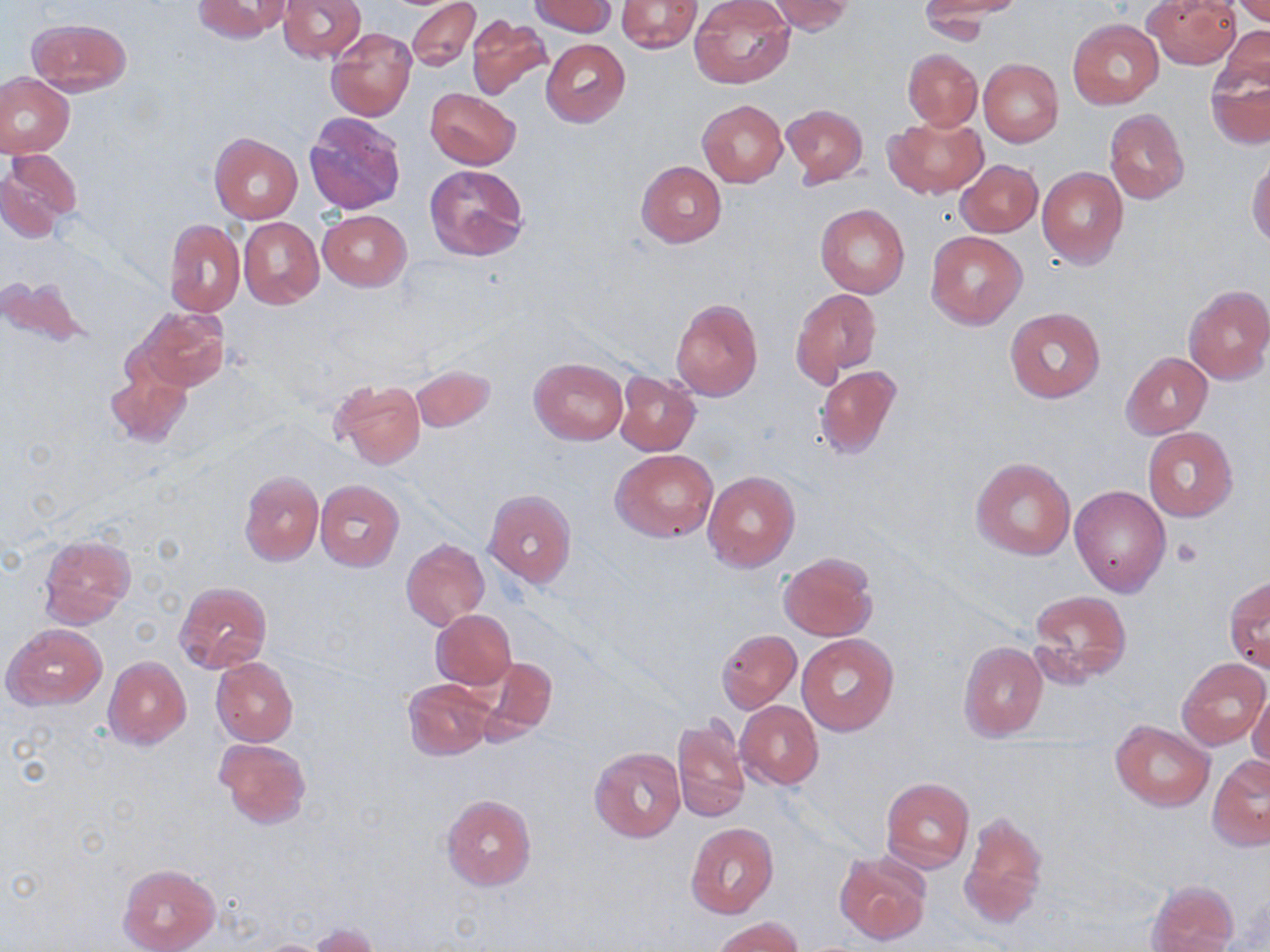

Summary:
  - Coordinate format: approximate bounding boxes as [x1, y1, x2, y2] in pixels
  - Uninfected red blood cell locations: [191, 0, 290, 43], [278, 0, 366, 63], [407, 0, 481, 72], [765, 0, 854, 35], [922, 0, 1026, 18], [1144, 0, 1241, 69], [1231, 0, 1270, 24], [529, 1, 615, 37], [616, 1, 702, 52], [689, 1, 794, 88], [917, 4, 1012, 41], [466, 14, 554, 102], [27, 17, 131, 96], [1068, 19, 1163, 109], [326, 27, 416, 121], [1214, 27, 1270, 96], [540, 39, 631, 127], [902, 48, 982, 130], [1207, 55, 1269, 151], [978, 57, 1063, 147], [0, 73, 74, 157], [425, 88, 521, 169], [697, 100, 788, 186], [782, 103, 867, 185], [1104, 108, 1190, 205], [304, 111, 406, 214], [885, 116, 987, 198], [210, 134, 302, 224], [2, 150, 81, 236], [1247, 153, 1270, 247], [957, 159, 1043, 238], [636, 161, 727, 247], [424, 163, 530, 261], [1037, 166, 1128, 269], [815, 204, 909, 297], [318, 210, 411, 291], [239, 216, 324, 309], [164, 219, 245, 316], [925, 231, 1028, 330], [0, 274, 88, 350], [1183, 285, 1270, 384], [791, 288, 882, 384], [671, 298, 763, 400], [1004, 306, 1106, 404], [133, 307, 230, 392], [1121, 352, 1213, 438], [530, 358, 629, 445], [104, 361, 191, 448], [410, 364, 495, 432], [812, 364, 902, 462], [615, 371, 700, 458], [331, 378, 426, 468], [1142, 427, 1238, 521], [611, 448, 717, 542], [971, 457, 1076, 562], [703, 470, 799, 571], [238, 471, 323, 565], [315, 481, 405, 572], [1069, 484, 1171, 598], [484, 489, 576, 586], [37, 534, 134, 627], [402, 538, 489, 630], [779, 553, 877, 641], [1225, 575, 1269, 673], [174, 581, 271, 677], [1028, 590, 1132, 683], [431, 609, 517, 690], [4, 624, 108, 710], [715, 629, 801, 712], [796, 634, 899, 736], [959, 641, 1049, 742], [103, 656, 191, 749], [473, 656, 557, 741], [1177, 656, 1268, 750], [211, 657, 298, 747], [403, 678, 496, 759], [1248, 688, 1270, 773], [736, 701, 823, 788], [671, 717, 751, 825], [1110, 720, 1213, 810], [216, 737, 312, 828], [589, 746, 685, 841], [1208, 755, 1270, 852], [881, 777, 974, 873], [441, 794, 536, 890], [960, 813, 1047, 929], [686, 822, 778, 918], [833, 852, 932, 945], [117, 862, 220, 952], [1147, 879, 1239, 952], [713, 916, 804, 952], [309, 922, 378, 951]
  - Platelet locations: [1173, 536, 1203, 568]
  - Slide-level diagnosis: no evidence of blood parasites
  - Preparation: thin blood film
  - Modality: optical microscopy
  - Magnification: 1000x
  - Stain: May-Grünwald-Giemsa
  - Image size: 1270×952 pixels
  - Field of view: single